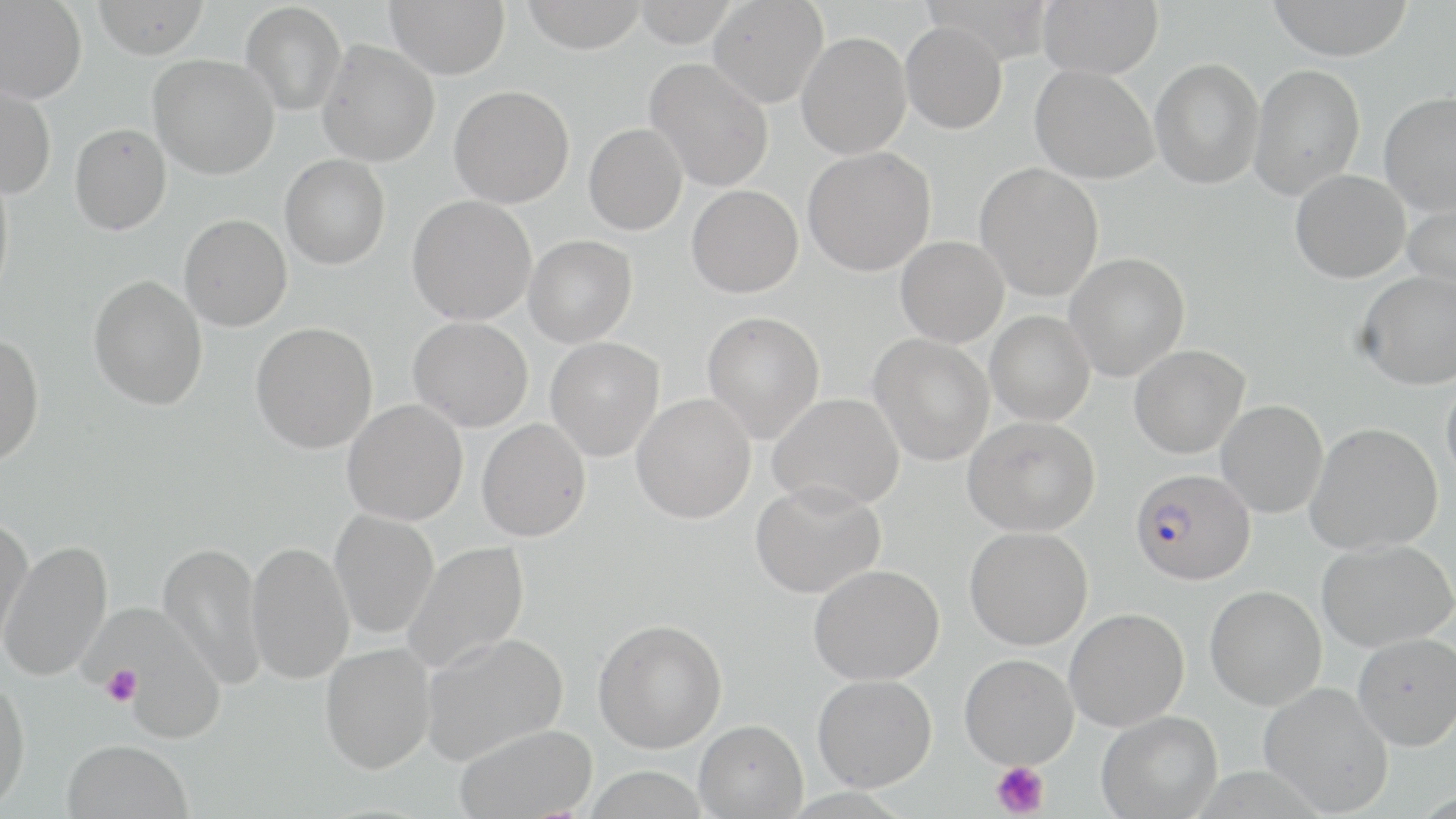
slide-level diagnosis = Plasmodium falciparum
magnification = 1000x
uninfected red blood cell locations = approximate bounding boxes as named x1/y1/x2/y2 corners in pixels: (x1=92, y1=0, x2=209, y2=59), (x1=386, y1=0, x2=509, y2=79), (x1=521, y1=0, x2=648, y2=53), (x1=632, y1=0, x2=738, y2=47), (x1=708, y1=0, x2=828, y2=107), (x1=1038, y1=0, x2=1163, y2=79), (x1=1267, y1=0, x2=1414, y2=60), (x1=0, y1=1, x2=87, y2=103), (x1=241, y1=2, x2=347, y2=116), (x1=900, y1=21, x2=1007, y2=134), (x1=796, y1=32, x2=911, y2=159), (x1=317, y1=40, x2=440, y2=167), (x1=148, y1=54, x2=279, y2=180), (x1=645, y1=58, x2=774, y2=191), (x1=1149, y1=59, x2=1264, y2=189), (x1=1249, y1=63, x2=1366, y2=200), (x1=1029, y1=64, x2=1159, y2=184), (x1=0, y1=84, x2=56, y2=198), (x1=449, y1=85, x2=574, y2=208), (x1=1378, y1=92, x2=1456, y2=216), (x1=69, y1=123, x2=172, y2=235), (x1=583, y1=123, x2=687, y2=235), (x1=802, y1=147, x2=935, y2=276), (x1=279, y1=154, x2=390, y2=269), (x1=975, y1=162, x2=1104, y2=302), (x1=0, y1=164, x2=14, y2=306), (x1=1290, y1=169, x2=1410, y2=283), (x1=687, y1=185, x2=803, y2=298), (x1=407, y1=195, x2=537, y2=325), (x1=1403, y1=196, x2=1456, y2=297), (x1=179, y1=213, x2=292, y2=331), (x1=524, y1=235, x2=637, y2=348), (x1=895, y1=236, x2=1008, y2=347), (x1=1065, y1=252, x2=1190, y2=382), (x1=1356, y1=271, x2=1456, y2=390), (x1=88, y1=274, x2=208, y2=411), (x1=702, y1=311, x2=825, y2=445), (x1=985, y1=311, x2=1095, y2=426), (x1=407, y1=316, x2=533, y2=432), (x1=251, y1=322, x2=378, y2=454), (x1=0, y1=331, x2=44, y2=466), (x1=869, y1=334, x2=994, y2=466), (x1=545, y1=336, x2=665, y2=461), (x1=1129, y1=345, x2=1250, y2=459), (x1=1441, y1=373, x2=1456, y2=490), (x1=767, y1=392, x2=904, y2=512), (x1=631, y1=393, x2=757, y2=523), (x1=343, y1=399, x2=468, y2=525), (x1=1216, y1=399, x2=1329, y2=518), (x1=962, y1=415, x2=1099, y2=536), (x1=477, y1=419, x2=591, y2=542), (x1=1307, y1=422, x2=1443, y2=555), (x1=750, y1=480, x2=886, y2=599), (x1=329, y1=509, x2=439, y2=640), (x1=0, y1=515, x2=33, y2=656), (x1=964, y1=526, x2=1093, y2=650), (x1=1316, y1=538, x2=1456, y2=651), (x1=0, y1=540, x2=112, y2=682), (x1=158, y1=540, x2=268, y2=690), (x1=245, y1=541, x2=354, y2=685), (x1=402, y1=541, x2=530, y2=675), (x1=808, y1=564, x2=944, y2=685), (x1=1205, y1=585, x2=1327, y2=710), (x1=89, y1=603, x2=224, y2=741), (x1=1064, y1=607, x2=1189, y2=732), (x1=593, y1=618, x2=727, y2=753), (x1=419, y1=632, x2=569, y2=765), (x1=1353, y1=632, x2=1456, y2=750), (x1=319, y1=643, x2=435, y2=774), (x1=959, y1=653, x2=1079, y2=769), (x1=812, y1=674, x2=937, y2=792), (x1=0, y1=677, x2=30, y2=815), (x1=1258, y1=681, x2=1394, y2=816), (x1=1096, y1=711, x2=1222, y2=819), (x1=693, y1=718, x2=808, y2=818), (x1=454, y1=723, x2=597, y2=819), (x1=62, y1=739, x2=193, y2=819), (x1=584, y1=766, x2=710, y2=819)
modality = optical microscopy
Plasmodium falciparum-infected red blood cell locations = approximate bounding boxes as named x1/y1/x2/y2 corners in pixels: (x1=1130, y1=468, x2=1256, y2=585)
image size = 1456×819 pixels
field of view = one of a larger specimen
preparation = thin blood film
stain = May-Grünwald-Giemsa
platelet locations = approximate bounding boxes as named x1/y1/x2/y2 corners in pixels: (x1=101, y1=665, x2=142, y2=707), (x1=991, y1=761, x2=1050, y2=817)